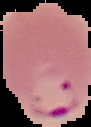

{
  "preparation": "thin blood film",
  "image_size": "91×127 pixels",
  "malaria_status": "parasitized",
  "image_type": "segmented cell region with the area outside set to black"
}